Name the blood parasite species.
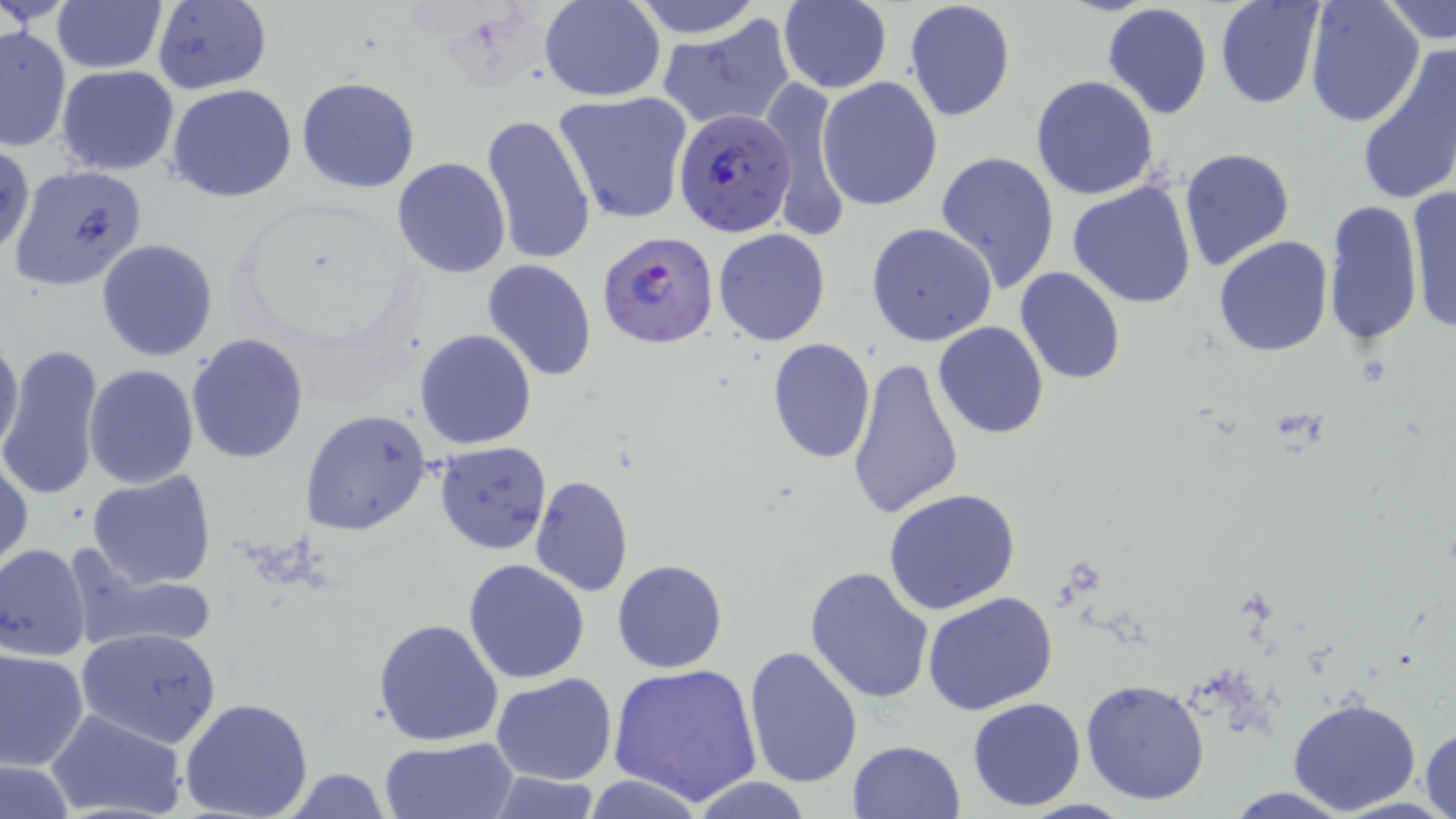
Plasmodium falciparum.

Approximate bounding boxes as (x1,y1)-(x2,y2) corner pairs in pixels. Uninfected red blood cell locations: (630,0)-(766,37), (49,1)-(167,72), (152,1)-(272,95), (539,1)-(666,101), (903,1)-(1016,121), (1213,1)-(1327,110), (1304,1)-(1425,128), (778,2)-(893,93), (1384,2)-(1456,51), (1100,3)-(1215,120), (658,15)-(796,133), (0,24)-(70,153), (1354,40)-(1456,209), (56,65)-(180,175), (1030,75)-(1159,200), (296,76)-(421,193), (817,76)-(945,213), (763,80)-(853,242), (167,84)-(296,202), (553,90)-(694,225), (481,112)-(596,266), (1,141)-(34,261), (1179,147)-(1295,272), (934,151)-(1060,293), (392,157)-(509,278), (12,164)-(147,291), (1067,178)-(1198,310), (1403,184)-(1456,336), (1323,200)-(1423,346), (866,223)-(997,347), (713,228)-(831,346), (1213,236)-(1333,357), (96,239)-(219,362), (481,260)-(598,383), (1015,266)-(1126,384), (932,322)-(1050,439), (414,329)-(537,450), (0,331)-(23,462), (185,334)-(310,463), (767,337)-(875,464), (1,344)-(105,500), (844,356)-(964,520), (84,364)-(199,487), (302,408)-(433,538), (434,441)-(553,555), (0,453)-(33,570), (87,470)-(217,590), (529,474)-(635,597), (884,487)-(1023,613), (0,543)-(92,662), (63,545)-(222,656), (463,558)-(592,684), (613,560)-(727,673), (803,565)-(934,705), (923,592)-(1057,714), (372,618)-(504,747), (77,627)-(223,747), (744,644)-(864,790), (0,647)-(88,770), (606,663)-(764,807), (491,672)-(618,785), (1080,677)-(1211,806), (1287,695)-(1422,815), (967,697)-(1086,810), (179,698)-(314,819), (45,709)-(188,819), (1418,727)-(1455,819), (378,737)-(519,819), (846,740)-(966,819), (0,757)-(76,819), (277,767)-(395,819), (485,770)-(603,818), (583,776)-(707,818), (688,777)-(815,818), (1220,787)-(1360,818). Plasmodium falciparum-infected red blood cell locations: (674,109)-(797,239), (597,229)-(720,349). One field of a larger specimen. Light microscopy. Image is 1456×819 pixels. May-Grünwald-Giemsa stain. Thin blood film. 1000x magnification.